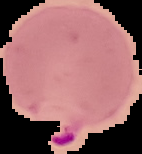 Malaria status: parasitized. Image is 142×154 pixels. From a thin blood smear. Cell region segmented out of the field of view; the surrounding area is masked to black.